Assess the morphology of the erythrocytes.
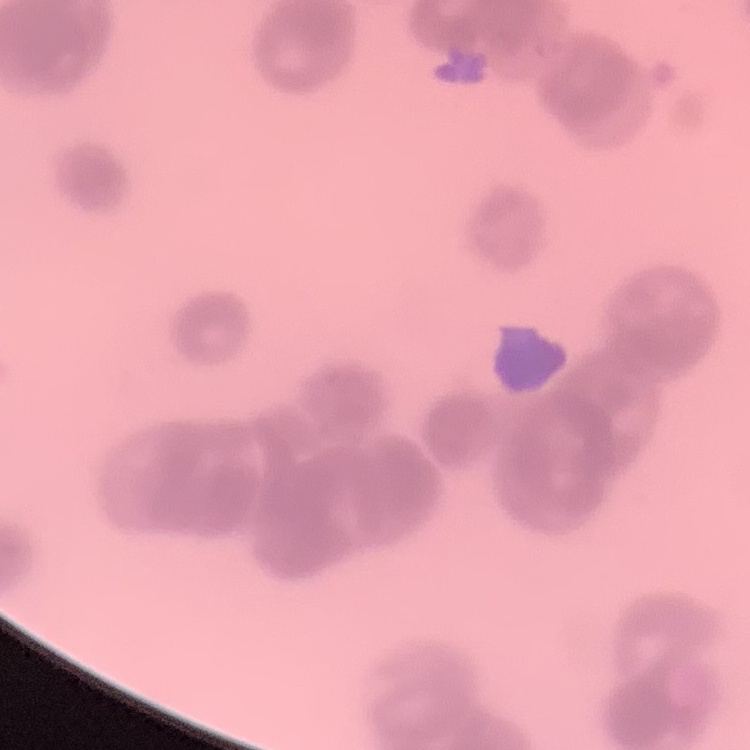
They show rouleaux formation.

Summary:
  - Image type: square crop of a larger photomicrograph
  - Preparation: thin peripheral smear
  - Stain: Field's or Giemsa